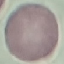
result: no malaria parasites seen
stain: Giemsa
image_type: automatically extracted cell patch, resized to 64 × 64 pixels
preparation: thin smear
capture: smartphone through the microscope eyepiece